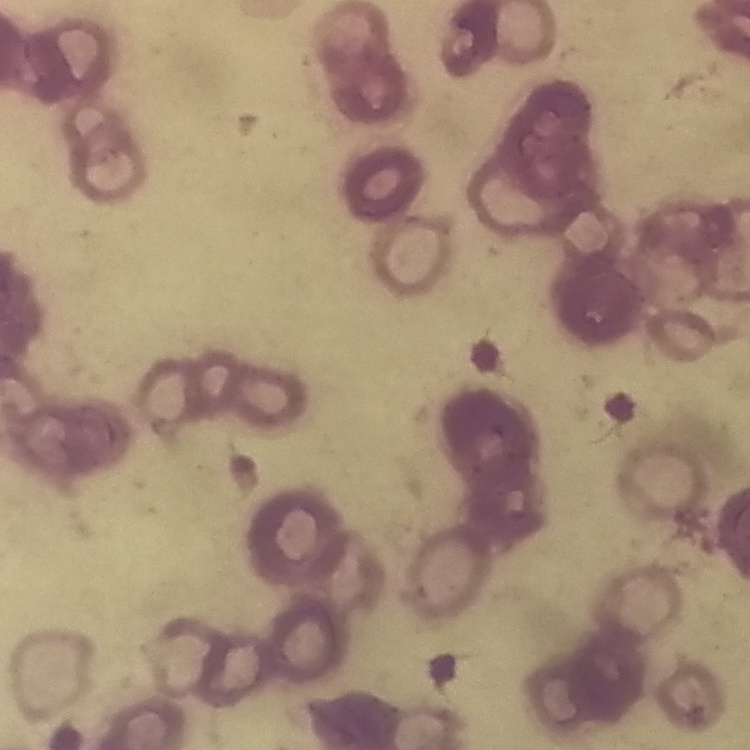 The erythrocytes exhibit rouleaux formation. Thin blood film. Stained with either Field's or Giemsa. Square crop of a larger photomicrograph.